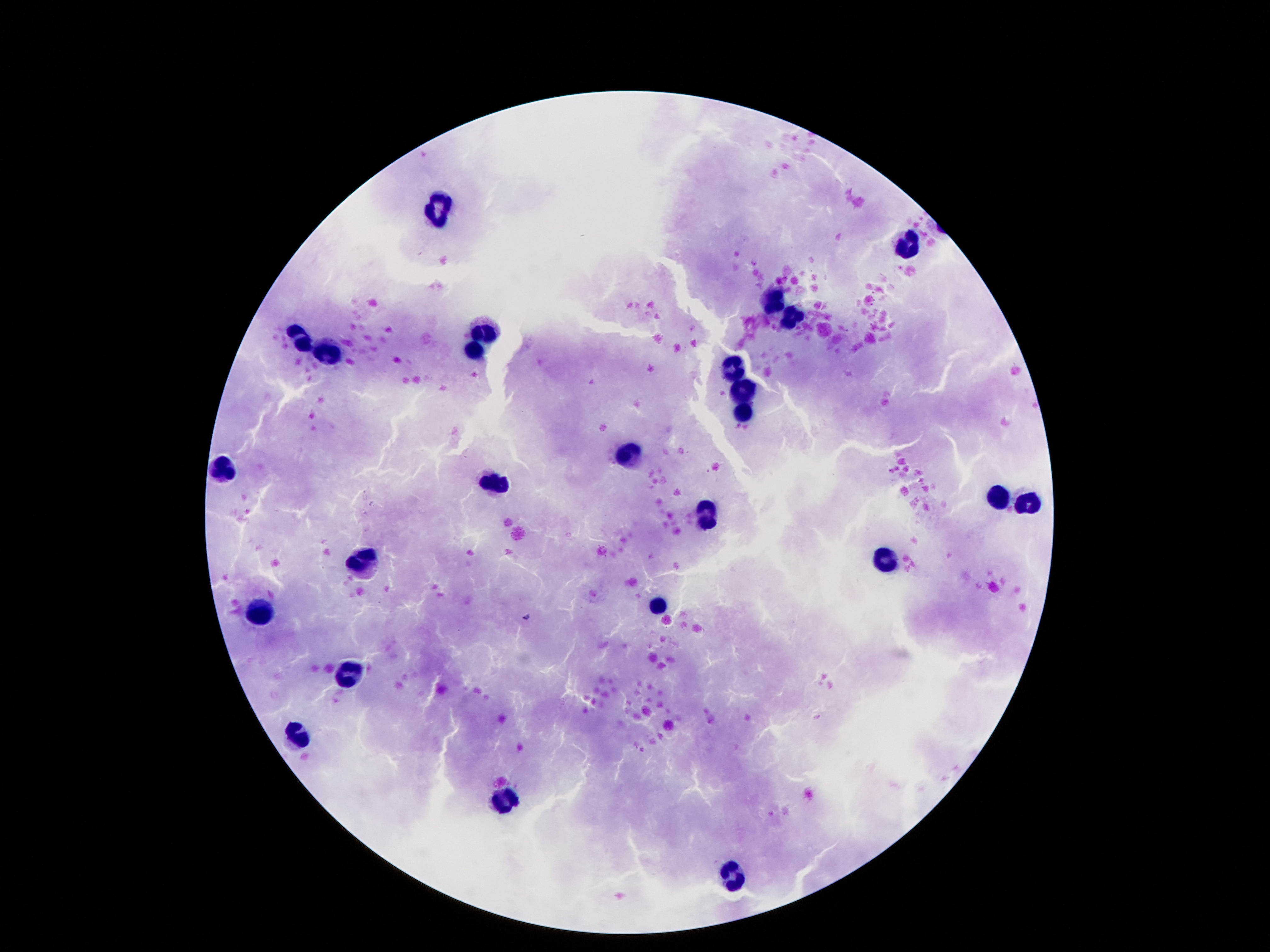

{
  "field_of_view": "one from this slide",
  "stain": "Giemsa",
  "capture": "smartphone camera through the microscope eyepiece",
  "preparation": "thick blood film",
  "magnification": "100x",
  "image_size": "1270×952 pixels",
  "leukocyte_locations": "approximate centers as (x, y) in pixels: (439, 209), (911, 250), (777, 304), (795, 318), (484, 330), (299, 338), (476, 349), (331, 354), (733, 367), (743, 391), (743, 412), (627, 454), (225, 468), (495, 483), (998, 496), (1028, 504), (706, 514), (888, 558), (364, 561), (660, 607), (263, 613), (349, 674), (298, 737), (504, 803), (731, 876)",
  "patient_malaria_status": "uninfected"
}